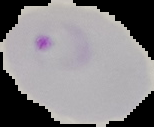

image_size: 154×127 pixels
malaria_status: parasitized
preparation: thin blood smear
image_type: segmented cell region on a black background